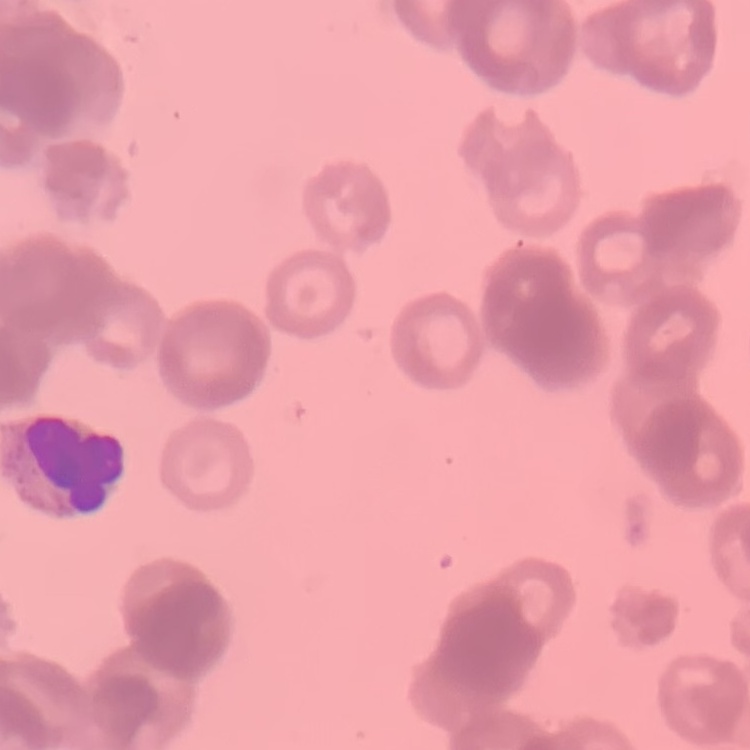
erythrocyte morphology = rouleaux formation
image type = square crop of a larger photomicrograph
preparation = thin blood film
stain = Field's or Giemsa